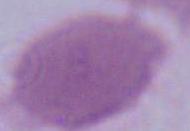
Captured at 1000x magnification. A red blood cell is shown. Micrograph.